Outline each blood parasite and name the species.
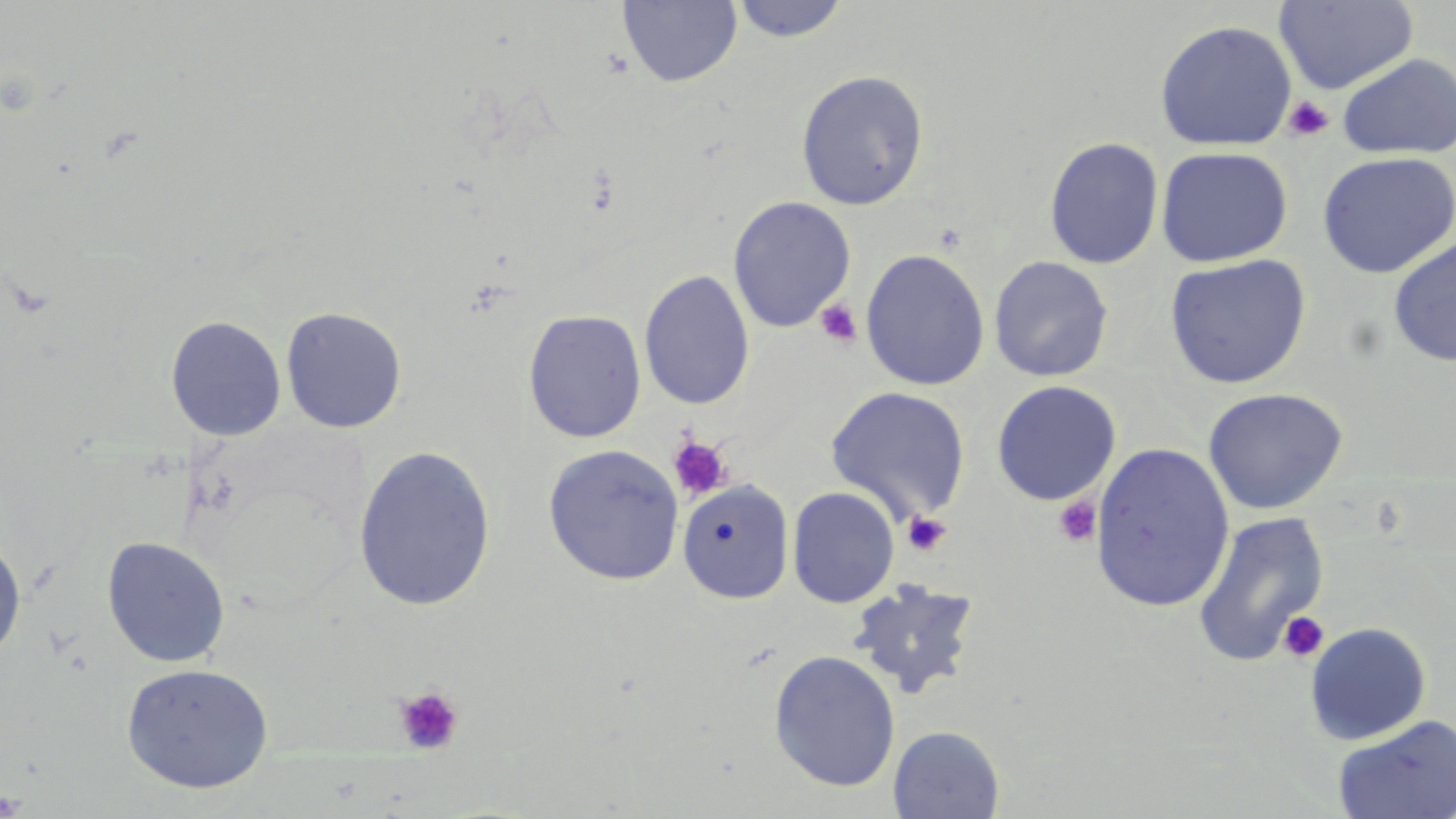

No blood parasites observed.

{
  "slide_level_diagnosis": "no evidence of blood parasites",
  "image_size": "1456×819 pixels",
  "uninfected_red_blood_cell_locations": "approximate bounding boxes as (x1,y1)-(x2,y2) corner pairs in pixels: (617,0)-(742,88), (729,0)-(851,43), (1275,1)-(1418,94), (1154,19)-(1297,151), (1337,53)-(1456,160), (795,69)-(929,210), (1043,136)-(1165,269), (1155,146)-(1293,267), (1317,152)-(1456,278), (728,195)-(856,332), (1388,236)-(1456,367), (860,249)-(990,391), (1164,254)-(1311,389), (988,255)-(1113,382), (639,268)-(755,411), (280,306)-(407,433), (523,309)-(647,443), (165,314)-(287,441), (990,380)-(1122,506), (825,386)-(972,522), (1202,387)-(1349,515), (1089,442)-(1234,612), (353,444)-(496,612), (543,444)-(684,585), (679,481)-(798,605), (787,486)-(900,608), (1192,510)-(1330,667), (0,535)-(26,662), (101,536)-(231,668), (847,577)-(983,699), (1304,622)-(1431,745), (768,649)-(901,791), (120,661)-(275,794), (1331,714)-(1456,819), (888,725)-(1006,818)",
  "field_of_view": "one of a larger specimen",
  "stain": "May-Grünwald-Giemsa",
  "modality": "optical microscopy",
  "preparation": "thin blood smear",
  "platelet_locations": "approximate bounding boxes as (x1,y1)-(x2,y2) corner pairs in pixels: (1283,95)-(1335,142), (815,299)-(862,348), (667,435)-(734,503), (1054,497)-(1102,547), (902,512)-(952,557), (1278,611)-(1330,663), (393,686)-(464,755), (0,789)-(28,817)",
  "magnification": "1000x"
}